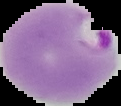

image size = 121×106 pixels
image type = segmented cell region on a black background
preparation = thin blood smear
malaria status = parasitized